Classify this cell by malaria status.
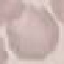
It is uninfected.

Thin blood smear. Automatically extracted cell patch, resized to 64 × 64 pixels. Acquired by smartphone through the microscope eyepiece. Giemsa-stained preparation.